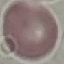
{
  "malaria_status": "uninfected",
  "capture": "smartphone through the microscope eyepiece",
  "image_type": "cell patch, automatically extracted from a larger field of view and resized to 64 × 64 pixels",
  "preparation": "thin blood smear",
  "stain": "Giemsa"
}